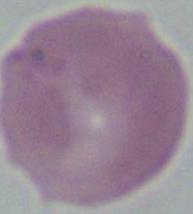

modality = photomicrograph
magnification = 1000x
identification = erythrocyte